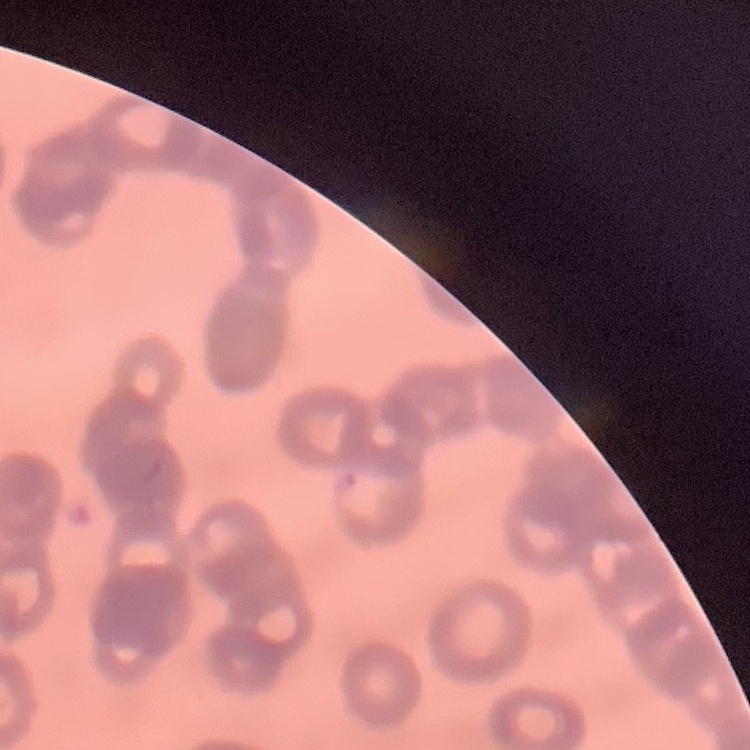

red blood cell morphology = rouleaux formation
image type = square crop of a larger photomicrograph
preparation = thin blood smear
stain = Field's or Giemsa